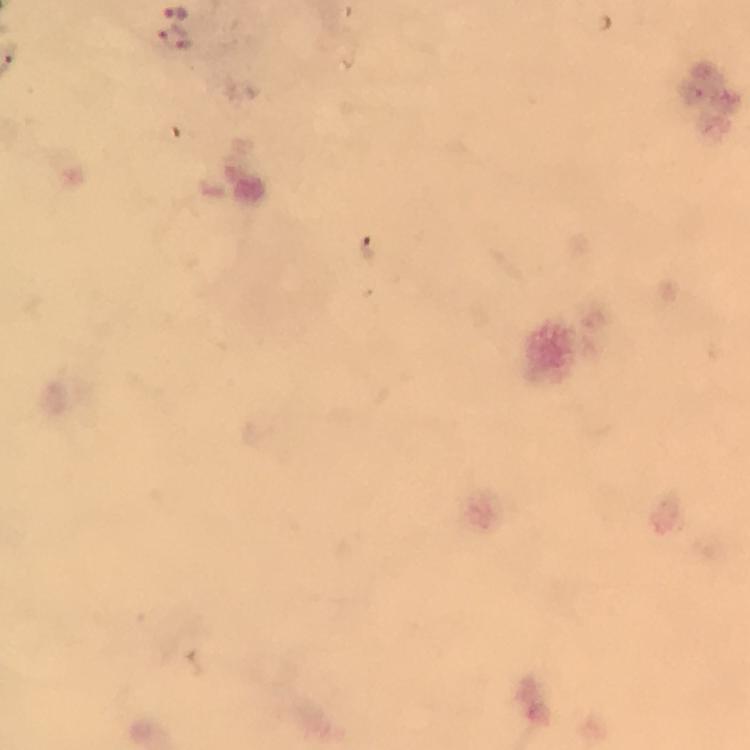
context: from a diagnostic examination for malaria
preparation: thick blood smear
magnification: 100x
stain: Giemsa
image_size: 750×750 pixels
malaria_parasite_locations: 'approximate centers as {x, y} in pixels: {175, 11}'
immersion_oil: used
capture: smartphone mounted on the microscope
cropped_from: a single field of view